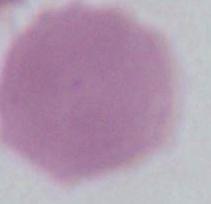
1000x magnification. An erythrocyte is shown. Micrograph.